Assess this cell for malaria.
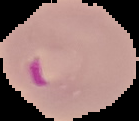
It is parasitized.

Summary:
  - Image type: segmented cell region on a black background
  - Image size: 139×121 pixels
  - Preparation: thin blood film